Classify this cell by malaria status.
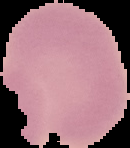

Uninfected.

Image is 130×148 pixels. The area outside the segmented cell region is set to black. From a thin blood film.